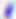
{
  "identification": "Toxoplasma gondii",
  "modality": "photomicrograph",
  "magnification": "400x"
}